Name the parasite shown.
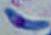

This is Toxoplasma gondii.

Summary:
  - Modality: micrograph
  - Magnification: 1000x